Identify the blood parasite species.
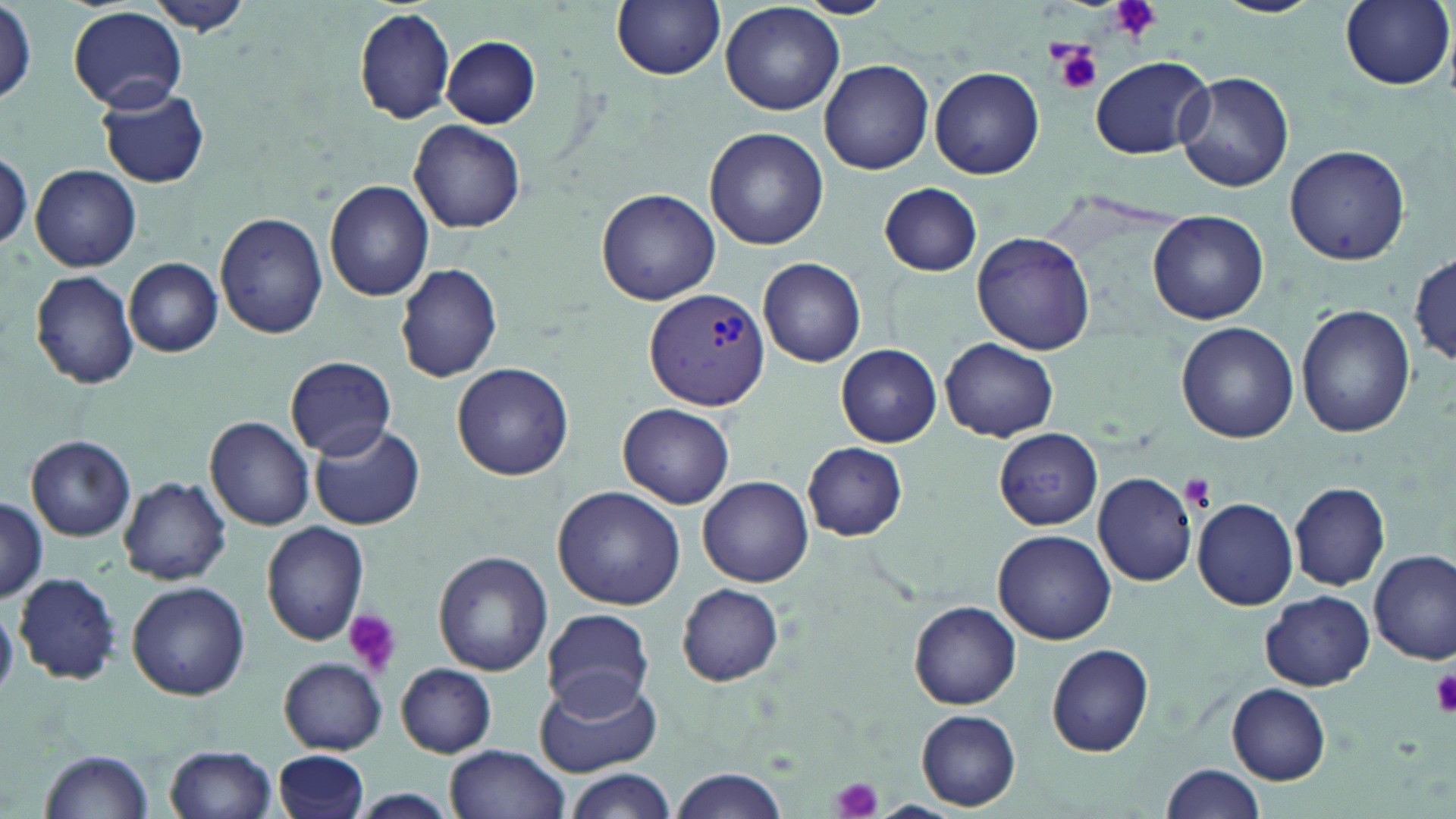

Plasmodium vivax.

Summary:
  - Coordinate format: approximate bounding boxes as named x1/y1/x2/y2 corners in pixels
  - Plasmodium vivax-infected red blood cell locations: (x1=644, y1=288, x2=771, y2=410)
  - Uninfected red blood cell locations: (x1=611, y1=0, x2=726, y2=80), (x1=797, y1=0, x2=895, y2=18), (x1=1212, y1=0, x2=1323, y2=17), (x1=1339, y1=0, x2=1453, y2=91), (x1=720, y1=1, x2=845, y2=115), (x1=145, y1=2, x2=254, y2=37), (x1=2, y1=5, x2=37, y2=108), (x1=70, y1=5, x2=187, y2=111), (x1=353, y1=7, x2=457, y2=124), (x1=443, y1=36, x2=540, y2=127), (x1=1091, y1=56, x2=1211, y2=158), (x1=818, y1=60, x2=934, y2=175), (x1=930, y1=66, x2=1045, y2=179), (x1=1175, y1=70, x2=1292, y2=192), (x1=98, y1=86, x2=210, y2=189), (x1=409, y1=120, x2=525, y2=233), (x1=704, y1=127, x2=829, y2=250), (x1=1284, y1=143, x2=1411, y2=266), (x1=0, y1=151, x2=31, y2=250), (x1=30, y1=164, x2=142, y2=272), (x1=322, y1=179, x2=435, y2=301), (x1=879, y1=183, x2=982, y2=275), (x1=596, y1=188, x2=721, y2=305), (x1=1148, y1=210, x2=1269, y2=325), (x1=214, y1=211, x2=330, y2=339), (x1=970, y1=231, x2=1096, y2=355), (x1=1410, y1=255, x2=1454, y2=366), (x1=758, y1=257, x2=866, y2=365), (x1=125, y1=258, x2=224, y2=357), (x1=392, y1=262, x2=503, y2=384), (x1=30, y1=269, x2=140, y2=389), (x1=1295, y1=304, x2=1416, y2=438), (x1=1177, y1=322, x2=1299, y2=443), (x1=941, y1=338, x2=1058, y2=441), (x1=835, y1=343, x2=942, y2=448), (x1=285, y1=356, x2=397, y2=459), (x1=452, y1=363, x2=575, y2=482), (x1=235, y1=391, x2=360, y2=532), (x1=618, y1=402, x2=736, y2=509), (x1=205, y1=416, x2=316, y2=531), (x1=308, y1=423, x2=426, y2=531), (x1=994, y1=428, x2=1103, y2=530), (x1=25, y1=435, x2=136, y2=542), (x1=803, y1=442, x2=908, y2=540), (x1=1092, y1=472, x2=1198, y2=586), (x1=118, y1=476, x2=231, y2=585), (x1=698, y1=476, x2=813, y2=584), (x1=1290, y1=482, x2=1390, y2=591), (x1=552, y1=485, x2=686, y2=611), (x1=0, y1=496, x2=47, y2=605), (x1=1192, y1=496, x2=1298, y2=610), (x1=260, y1=521, x2=370, y2=646), (x1=993, y1=529, x2=1115, y2=643), (x1=1370, y1=549, x2=1455, y2=663), (x1=432, y1=551, x2=554, y2=677), (x1=13, y1=572, x2=120, y2=685), (x1=126, y1=580, x2=250, y2=700), (x1=676, y1=583, x2=785, y2=686), (x1=1261, y1=589, x2=1375, y2=690), (x1=909, y1=601, x2=1022, y2=709), (x1=541, y1=608, x2=654, y2=716), (x1=1047, y1=642, x2=1153, y2=758), (x1=278, y1=658, x2=388, y2=754), (x1=395, y1=664, x2=497, y2=757), (x1=535, y1=671, x2=661, y2=777), (x1=1227, y1=683, x2=1331, y2=784), (x1=917, y1=710, x2=1021, y2=810), (x1=445, y1=743, x2=570, y2=819), (x1=164, y1=744, x2=278, y2=819), (x1=41, y1=748, x2=153, y2=817), (x1=274, y1=750, x2=370, y2=819), (x1=1161, y1=763, x2=1266, y2=819), (x1=564, y1=769, x2=677, y2=819), (x1=669, y1=769, x2=788, y2=818), (x1=350, y1=789, x2=459, y2=818)
  - Platelet locations: (x1=1109, y1=0, x2=1162, y2=41), (x1=1050, y1=40, x2=1104, y2=97), (x1=1181, y1=475, x2=1215, y2=509), (x1=343, y1=609, x2=401, y2=676), (x1=1429, y1=666, x2=1456, y2=717), (x1=829, y1=776, x2=883, y2=819)
  - Image size: 1456×819 pixels
  - Stain: May-Grünwald-Giemsa
  - Magnification: 1000x
  - Modality: light microscopy
  - Field of view: one of a larger specimen
  - Preparation: thin blood smear